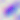

Toxoplasma gondii is shown. Photomicrograph. Captured at 400x magnification.